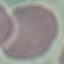

{
  "result": "no malaria parasites detected",
  "capture": "smartphone through the microscope eyepiece",
  "preparation": "thin smear",
  "stain": "Giemsa",
  "image_type": "cell patch, automatically extracted from a larger field of view and resized to 64 × 64 pixels"
}